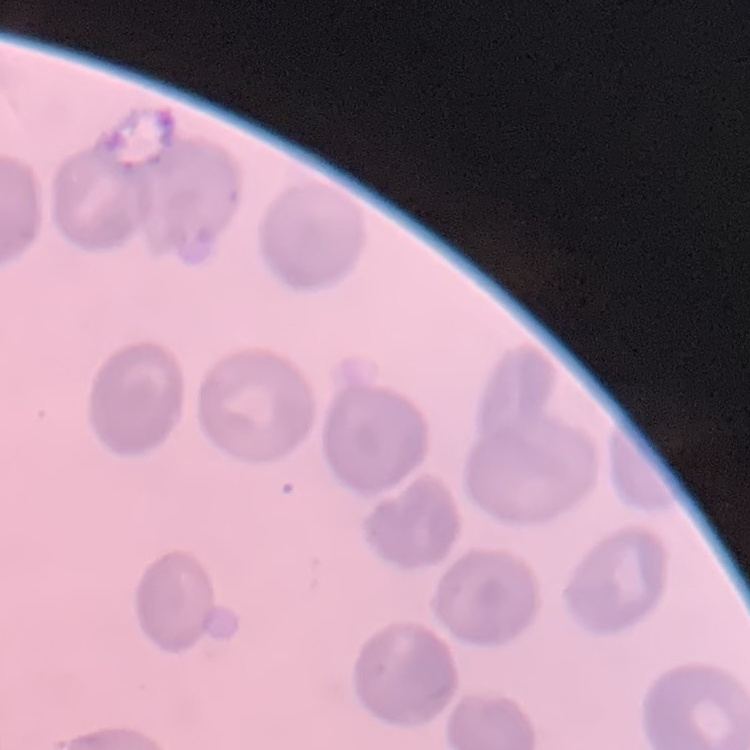 The erythrocytes exhibit no rouleaux formation. Square crop of a larger photomicrograph. Field's or Giemsa stain. Thin blood smear.